Give the extent of all uninfected red blood cells.
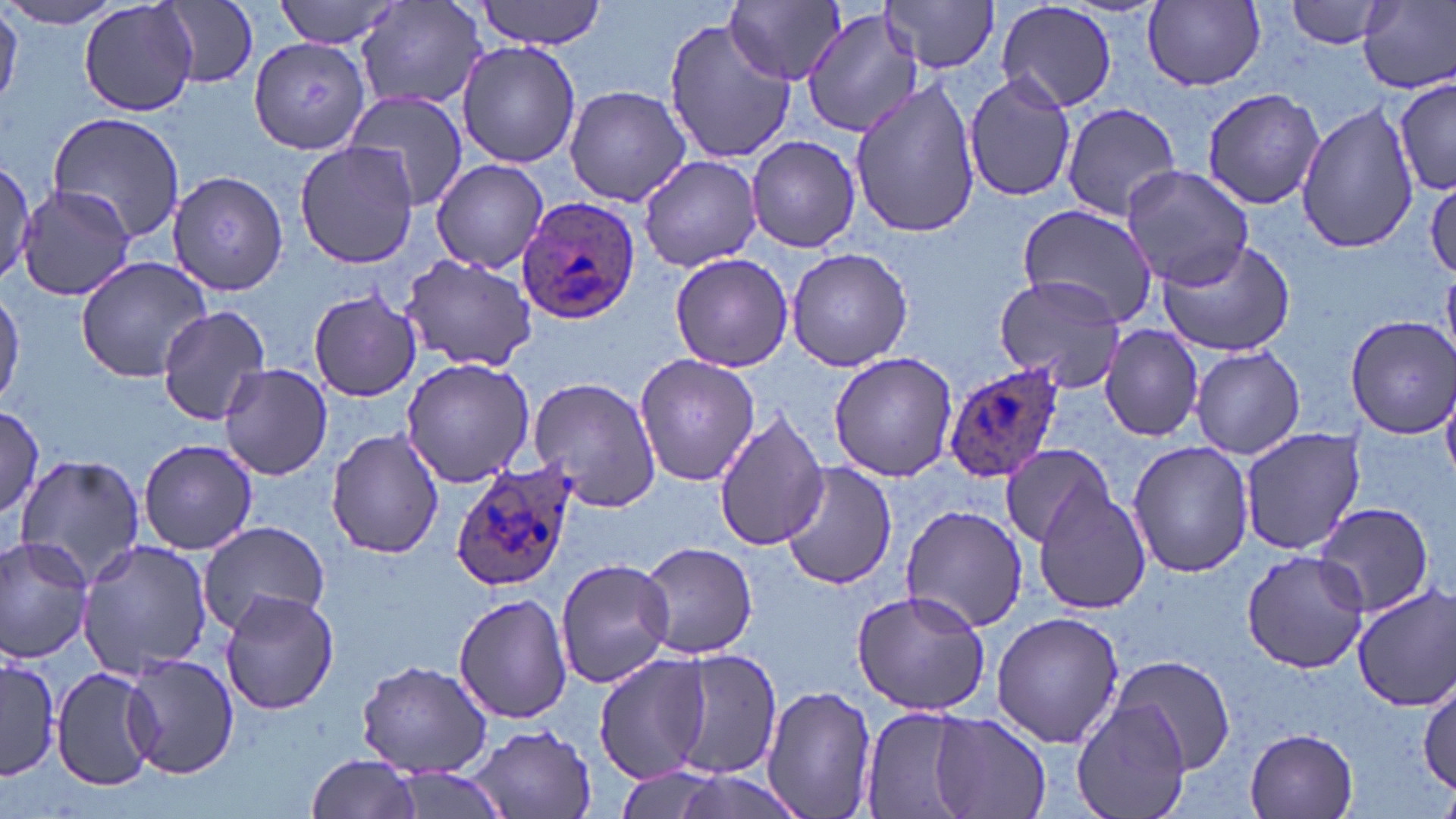
Approximate bounding boxes as (x1, y1, x2, y2) in pixels.
Uninfected red blood cells: (272, 0, 408, 51), (473, 0, 609, 50), (881, 0, 1001, 74), (1140, 0, 1269, 95), (0, 1, 125, 29), (0, 1, 22, 109), (79, 1, 197, 118), (726, 1, 843, 87), (995, 1, 1118, 114), (1285, 1, 1391, 49), (157, 2, 259, 88), (356, 2, 487, 113), (1359, 2, 1456, 93), (801, 3, 927, 139), (661, 14, 796, 168), (247, 36, 371, 153), (456, 42, 582, 169), (963, 71, 1078, 203), (1392, 73, 1453, 199), (850, 79, 982, 239), (563, 85, 693, 206), (1200, 87, 1325, 209), (341, 90, 467, 213), (1293, 102, 1418, 255), (1060, 103, 1182, 221), (47, 112, 189, 245), (746, 135, 860, 253), (294, 141, 418, 268), (640, 156, 763, 272), (431, 159, 550, 275), (0, 161, 35, 289), (1120, 165, 1254, 287), (169, 170, 289, 295), (1426, 178, 1456, 281), (16, 183, 137, 300), (1016, 204, 1156, 323), (1155, 239, 1296, 358), (785, 246, 913, 371), (669, 253, 795, 371), (399, 254, 537, 370), (76, 256, 213, 381), (1443, 269, 1456, 357), (992, 274, 1129, 392), (0, 284, 24, 409), (307, 289, 421, 402), (155, 306, 270, 425), (1347, 315, 1455, 438), (1100, 325, 1204, 441), (1190, 346, 1306, 459), (828, 352, 957, 482), (633, 355, 760, 485), (400, 358, 534, 485), (219, 362, 332, 481), (1201, 370, 1331, 526), (528, 377, 663, 512), (1442, 381, 1456, 486), (0, 407, 45, 516), (714, 407, 831, 553), (1238, 427, 1366, 556), (326, 428, 444, 560), (1127, 439, 1252, 577), (139, 440, 259, 556), (1001, 441, 1116, 547), (13, 452, 145, 584), (779, 462, 896, 591), (1033, 483, 1152, 615), (1314, 501, 1436, 617), (897, 503, 1030, 632), (196, 520, 329, 636), (0, 535, 97, 665), (76, 536, 215, 680), (636, 541, 759, 659), (1242, 549, 1369, 672), (554, 557, 674, 689), (1349, 585, 1456, 713), (850, 588, 990, 718), (220, 589, 338, 715), (453, 593, 573, 724), (991, 609, 1125, 748), (662, 646, 784, 782), (2, 653, 60, 781), (122, 653, 239, 779), (595, 654, 711, 782), (1111, 654, 1236, 772), (357, 660, 493, 778), (50, 666, 160, 791), (1418, 675, 1454, 801), (762, 684, 878, 819), (1073, 699, 1193, 819), (860, 707, 984, 819), (931, 713, 1049, 818), (462, 724, 600, 818), (1245, 728, 1360, 818), (305, 752, 424, 819).

Summary:
  - Plasmodium ovale-infected red blood cell locations: (513, 194, 642, 325), (945, 362, 1064, 483), (450, 458, 581, 594)
  - Slide-level diagnosis: Plasmodium ovale
  - Field of view: single
  - Image size: 1456×819 pixels
  - Preparation: thin blood smear
  - Magnification: 1000x
  - Modality: light microscopy
  - Stain: May-Grünwald-Giemsa